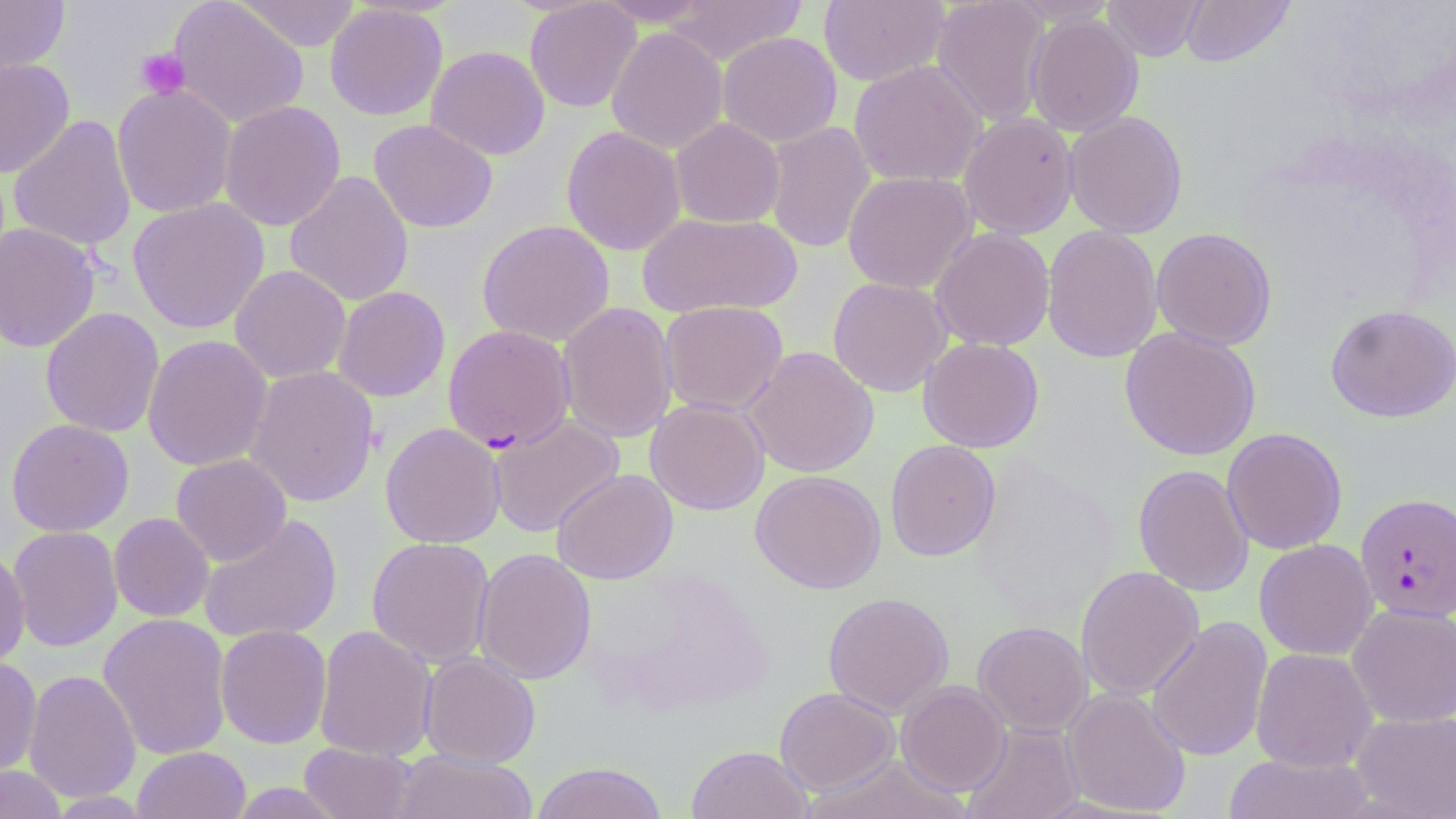

Summary:
  - Coordinate format: approximate bounding boxes as [x1, y1, x2, y2] in pixels
  - Uninfected red blood cell locations: [169, 0, 309, 128], [233, 0, 362, 52], [594, 0, 715, 26], [665, 0, 808, 65], [818, 0, 950, 87], [931, 0, 1051, 126], [1102, 0, 1206, 61], [1181, 0, 1294, 67], [0, 1, 69, 80], [524, 1, 642, 113], [325, 3, 448, 121], [1025, 13, 1144, 136], [607, 27, 728, 154], [718, 31, 842, 147], [426, 45, 550, 160], [0, 58, 75, 178], [849, 59, 986, 188], [112, 83, 237, 219], [219, 100, 346, 232], [1064, 110, 1188, 238], [958, 112, 1079, 240], [9, 115, 136, 253], [671, 118, 785, 228], [368, 119, 498, 233], [764, 121, 876, 254], [561, 126, 686, 255], [285, 170, 414, 307], [842, 171, 977, 293], [128, 198, 269, 334], [637, 212, 802, 318], [477, 219, 614, 346], [1, 222, 100, 352], [1042, 225, 1164, 363], [930, 227, 1055, 351], [1151, 227, 1277, 350], [229, 265, 351, 384], [827, 277, 951, 397], [333, 286, 450, 402], [659, 301, 788, 415], [557, 302, 678, 443], [1325, 304, 1456, 422], [40, 307, 164, 438], [1119, 326, 1261, 461], [142, 334, 272, 472], [918, 337, 1044, 453], [744, 346, 880, 478], [244, 365, 379, 507], [645, 398, 769, 515], [488, 415, 624, 537], [6, 418, 134, 537], [381, 422, 505, 548], [1222, 428, 1347, 555], [885, 439, 1001, 562], [171, 454, 292, 566], [1133, 464, 1254, 597], [552, 469, 678, 584], [750, 469, 886, 594], [109, 513, 214, 622], [199, 514, 342, 644], [7, 526, 123, 652], [367, 536, 495, 668], [1254, 539, 1378, 660], [474, 547, 596, 686], [0, 549, 30, 670], [1076, 565, 1204, 700], [822, 591, 955, 717], [1346, 603, 1456, 728], [98, 613, 232, 760], [1146, 616, 1273, 762], [972, 621, 1092, 736], [215, 624, 332, 748], [314, 625, 437, 761], [1250, 647, 1377, 772], [419, 651, 541, 768], [0, 656, 42, 778], [23, 669, 141, 803], [897, 681, 1011, 795], [774, 687, 899, 795], [1062, 687, 1191, 817], [1350, 711, 1456, 819], [962, 722, 1085, 819], [299, 743, 417, 819], [686, 745, 814, 819], [132, 746, 250, 819], [392, 751, 538, 819], [1221, 753, 1376, 818], [803, 754, 970, 819], [530, 762, 669, 819], [0, 765, 67, 819], [225, 782, 349, 818], [47, 791, 155, 818]
  - Platelet locations: [135, 47, 191, 99]
  - Plasmodium falciparum-infected red blood cell locations: [442, 324, 575, 452], [1355, 492, 1456, 622]
  - Slide-level diagnosis: Plasmodium falciparum
  - Stain: May-Grünwald-Giemsa
  - Magnification: 1000x
  - Preparation: thin blood smear
  - Image size: 1456×819 pixels
  - Modality: optical microscopy
  - Field of view: single